State which parasite is depicted.
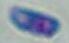

Toxoplasma gondii.

{
  "magnification": "1000x",
  "modality": "photomicrograph"
}